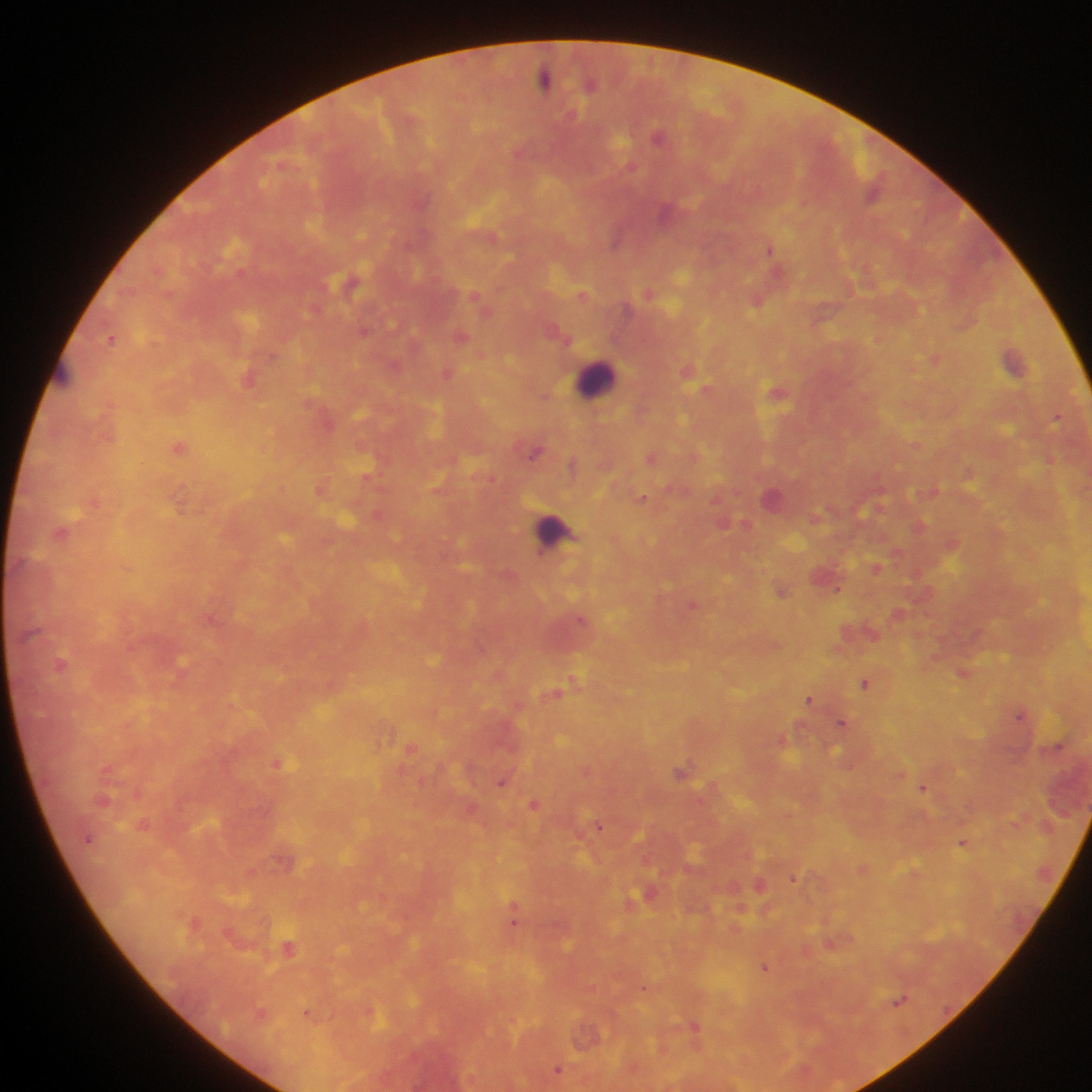
Approximate centers as [x, y] in pixels.
Summary:
  - Plasmodium parasite locations: [544, 79], [591, 84], [573, 115], [658, 137], [630, 167], [665, 214], [771, 250], [648, 293], [475, 294], [757, 302], [363, 330], [461, 336], [110, 338], [934, 359], [1013, 361], [395, 365], [448, 372], [1056, 417], [179, 447], [534, 453], [652, 457], [642, 498], [747, 524], [62, 532], [875, 567], [838, 588], [782, 591], [693, 604], [580, 619], [61, 664], [962, 672], [865, 683], [554, 693], [809, 700], [1020, 714], [841, 722], [278, 763], [106, 769], [681, 771], [501, 783], [922, 788], [103, 800], [533, 805], [599, 827], [88, 839], [962, 843], [793, 877], [512, 919], [288, 948], [765, 967], [643, 989], [900, 1000], [261, 1013], [307, 1014], [694, 1026], [557, 1069]
  - Leukocyte locations: [597, 379], [554, 532]
  - Capture: mobile-phone photograph through a microscope
  - Country: Ghana
  - Preparation: thick blood film
  - Field of view: single
  - Image size: 1092×1092 pixels